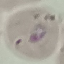
Result: malaria parasites identified. Photographed with a smartphone camera at the microscope eyepiece. Giemsa-stained preparation. Cell patch, automatically extracted from a larger field of view and resized to 64 × 64 pixels. Thin smear of blood.